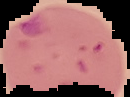

preparation: thin blood film
image_type: segmented cell region with the area outside set to black
result: malaria parasites detected
image_size: 130×97 pixels